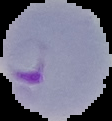

Result: malaria parasites identified. Segmented cell region on a black background. Image is 112×121 pixels. From a thin blood film.